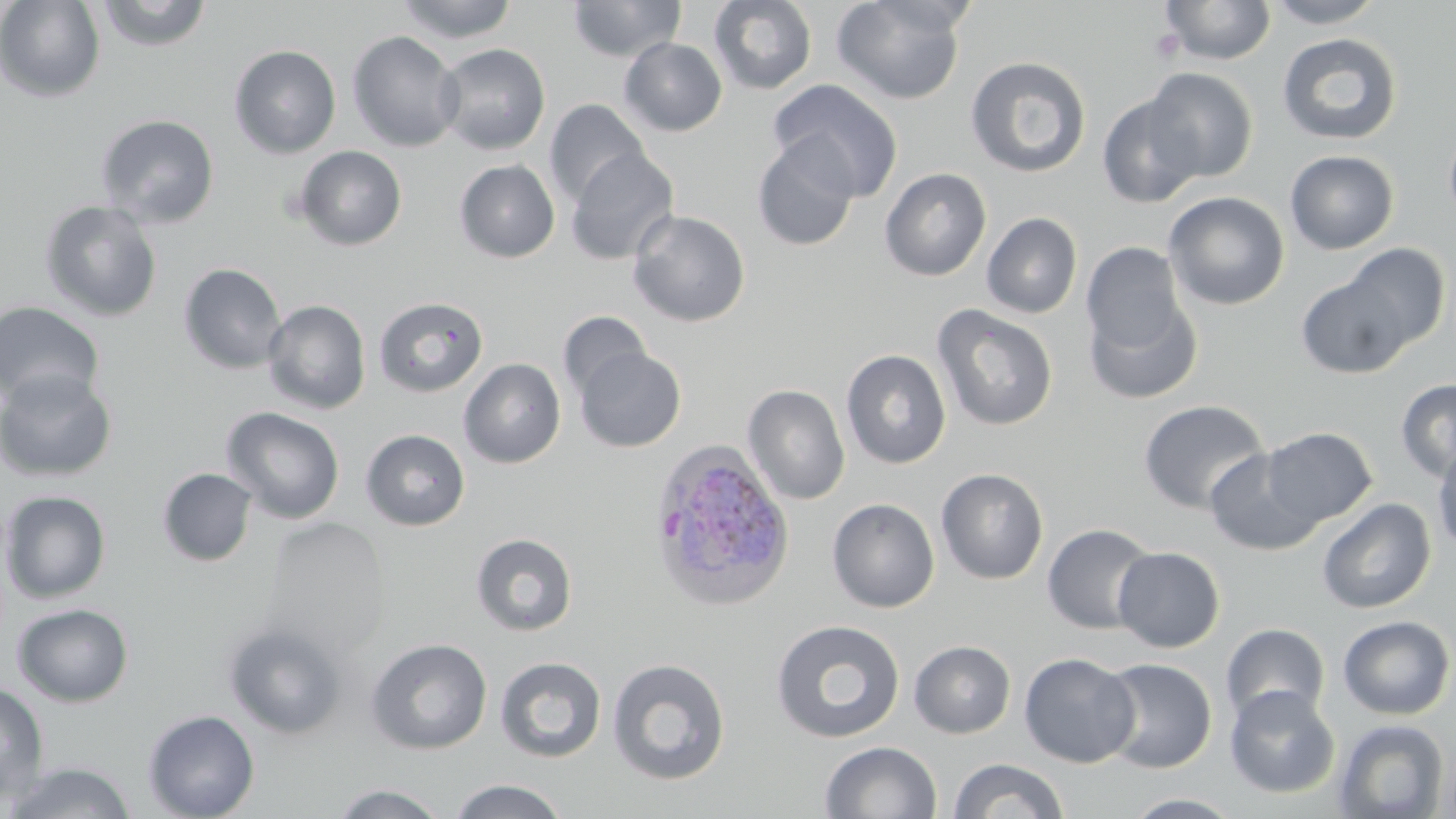
Summary:
  - Coordinate format: approximate bounding boxes as [x1, y1, x2, y2] in pixels
  - Uninfected red blood cell locations: [0, 0, 106, 102], [94, 0, 214, 51], [395, 0, 518, 43], [566, 0, 686, 62], [708, 0, 818, 95], [831, 0, 968, 105], [1159, 0, 1277, 65], [1263, 0, 1387, 29], [347, 31, 464, 152], [1276, 32, 1403, 145], [619, 38, 727, 136], [435, 43, 551, 155], [229, 44, 341, 158], [965, 56, 1092, 178], [1143, 67, 1258, 183], [768, 79, 904, 201], [1097, 94, 1205, 209], [545, 99, 650, 208], [95, 114, 220, 228], [1443, 125, 1456, 228], [751, 137, 860, 252], [294, 145, 407, 251], [566, 148, 678, 265], [1284, 150, 1399, 255], [454, 160, 560, 263], [879, 167, 991, 281], [1163, 191, 1290, 310], [39, 200, 163, 321], [627, 209, 750, 327], [982, 213, 1082, 318], [1081, 242, 1190, 364], [1342, 243, 1452, 352], [178, 263, 287, 374], [1295, 271, 1417, 380], [1083, 288, 1203, 405], [373, 296, 489, 398], [263, 299, 371, 414], [0, 301, 105, 410], [932, 304, 1058, 431], [558, 311, 652, 402], [575, 345, 688, 453], [841, 349, 951, 469], [459, 358, 566, 468], [0, 369, 118, 482], [1395, 379, 1456, 483], [743, 384, 850, 505], [1138, 400, 1269, 515], [221, 407, 345, 524], [1260, 427, 1378, 527], [360, 429, 470, 530], [1432, 441, 1456, 555], [1204, 448, 1323, 556], [157, 468, 258, 566], [935, 468, 1048, 585], [0, 490, 111, 604], [827, 497, 940, 613], [1317, 497, 1436, 614], [262, 518, 391, 659], [1042, 523, 1158, 634], [471, 532, 578, 636], [1112, 546, 1225, 652], [12, 602, 133, 707], [1337, 615, 1455, 720], [770, 619, 906, 744], [222, 622, 349, 740], [1220, 623, 1330, 725], [365, 638, 492, 755], [909, 640, 1016, 738], [1019, 652, 1140, 768], [496, 656, 606, 763], [607, 657, 731, 785], [1098, 658, 1218, 773], [0, 682, 49, 804], [1224, 686, 1340, 798], [143, 709, 260, 819], [1332, 718, 1449, 818], [819, 740, 942, 819], [949, 758, 1068, 818], [4, 761, 137, 818], [447, 779, 570, 819], [328, 783, 452, 818], [1122, 792, 1243, 818]
  - Plasmodium ovale-infected red blood cell locations: [648, 439, 796, 610]
  - Platelet locations: [1149, 28, 1184, 62]
  - Slide-level diagnosis: Plasmodium ovale
  - Magnification: 1000x
  - Field of view: one of a larger specimen
  - Image size: 1456×819 pixels
  - Preparation: thin blood smear
  - Stain: May-Grünwald-Giemsa
  - Modality: optical microscopy